Outline each Babesia divergens-infected red blood cell.
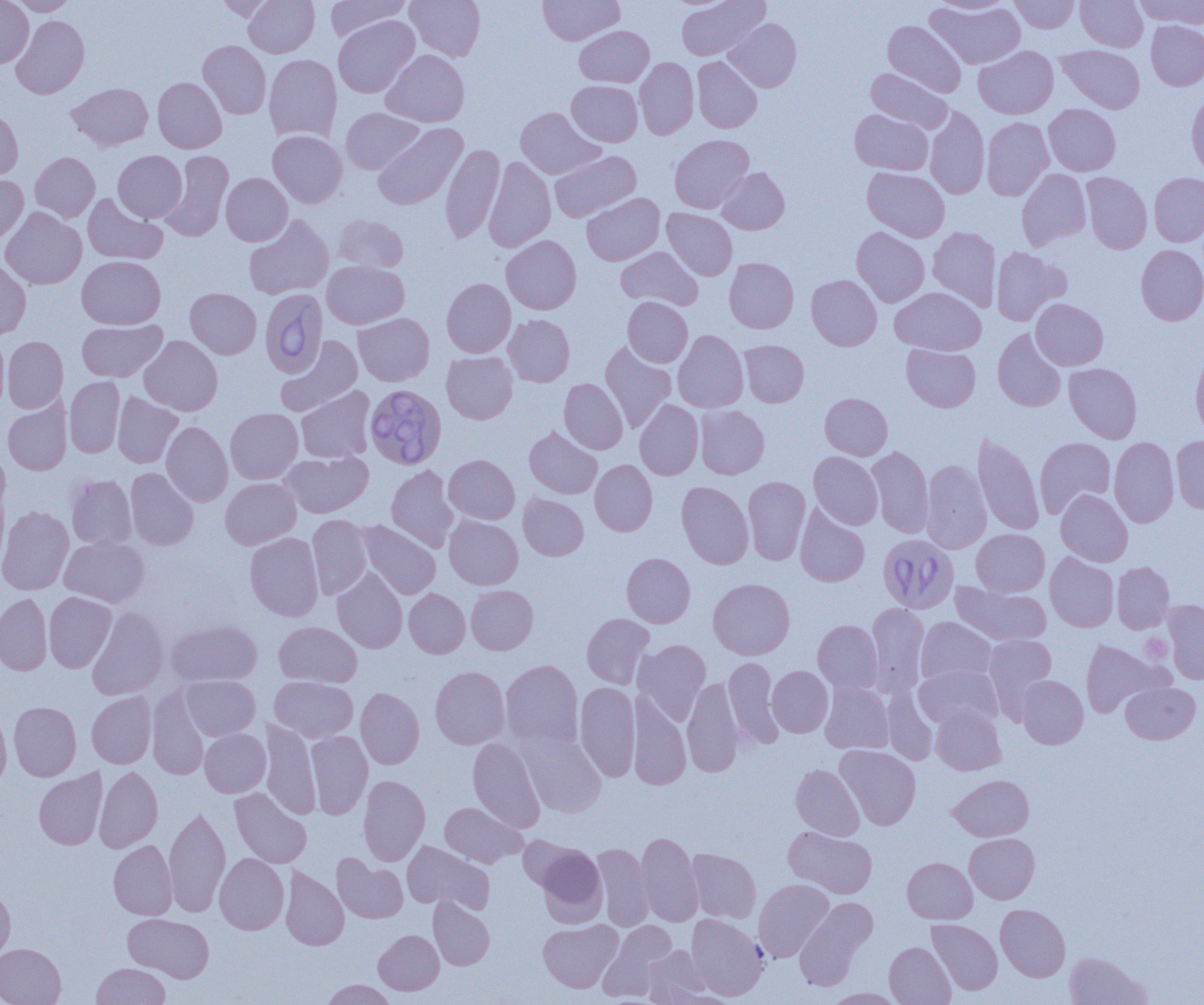
Approximate bounding boxes as (x1,y1)-(x2,y2) corner pairs in pixels.
Babesia divergens-infected red blood cells: (260,288)-(327,378), (365,384)-(446,469), (881,533)-(956,616).

slide-level diagnosis = Babesia divergens
modality = light microscopy
preparation = thin blood film
uninfected red blood cell locations = approximate bounding boxes as (x1,y1)-(x2,y2) corner pairs in pixels: (0,0)-(34,68), (9,0)-(77,15), (214,0)-(279,21), (243,0)-(319,57), (326,0)-(411,41), (405,0)-(485,61), (538,0)-(624,45), (676,0)-(769,60), (933,0)-(1014,14), (1009,0)-(1079,33), (1076,0)-(1148,52), (1134,0)-(1204,29), (925,1)-(1025,69), (11,15)-(90,99), (333,15)-(419,98), (724,18)-(801,92), (883,20)-(966,97), (1146,21)-(1204,90), (574,25)-(654,87), (198,40)-(271,119), (973,45)-(1058,118), (1057,45)-(1145,113), (381,50)-(469,127), (264,54)-(342,143), (692,56)-(762,133), (635,57)-(699,139), (866,69)-(952,133), (153,77)-(226,153), (567,80)-(642,146), (67,82)-(153,151), (1186,93)-(1204,180), (1044,104)-(1121,175), (925,106)-(989,199), (341,107)-(423,174), (515,107)-(604,179), (0,109)-(23,180), (849,109)-(933,175), (982,117)-(1054,200), (372,123)-(467,210), (268,130)-(347,208), (669,135)-(754,213), (441,143)-(505,244), (113,150)-(187,222), (160,150)-(233,242), (550,150)-(641,222), (30,152)-(100,222), (484,156)-(555,253), (717,167)-(789,234), (862,167)-(950,242), (1016,169)-(1091,250), (221,172)-(292,246), (1081,172)-(1152,254), (1149,172)-(1204,246), (0,175)-(28,244), (582,192)-(664,265), (82,193)-(167,265), (0,207)-(87,289), (662,208)-(737,280), (243,214)-(334,300), (334,215)-(409,272), (928,226)-(1001,311), (852,227)-(929,307), (501,235)-(581,315), (1136,244)-(1204,325), (616,246)-(703,310), (991,247)-(1070,325), (77,256)-(166,329), (0,257)-(31,340), (724,257)-(798,333), (322,260)-(409,329), (806,275)-(881,350), (441,278)-(516,357), (890,287)-(986,355), (185,288)-(261,359), (623,296)-(693,367), (1031,299)-(1108,370), (354,313)-(434,386), (504,314)-(574,386), (76,319)-(167,382), (992,329)-(1066,412), (673,330)-(748,413), (0,335)-(10,413), (139,335)-(223,415), (2,336)-(68,413), (275,336)-(362,417), (739,340)-(809,407), (599,341)-(676,432), (902,343)-(980,412), (1191,349)-(1204,438), (441,351)-(517,423), (1064,363)-(1142,443), (64,376)-(125,458), (559,378)-(628,454), (296,386)-(376,463), (113,391)-(183,468), (820,393)-(892,459), (2,398)-(72,475), (635,399)-(703,480), (695,405)-(769,478), (225,408)-(303,484), (161,421)-(233,507), (524,426)-(602,499), (973,433)-(1044,535), (1171,436)-(1204,513), (1035,437)-(1116,518), (1109,437)-(1179,528), (867,446)-(934,538), (281,450)-(373,518), (809,451)-(883,529), (444,454)-(520,524), (921,458)-(991,553), (590,460)-(657,536), (386,465)-(458,552), (125,467)-(199,550), (66,474)-(137,549), (743,476)-(810,564), (220,477)-(301,549), (676,481)-(753,569), (1055,489)-(1132,566), (518,493)-(588,560), (795,504)-(870,587), (0,506)-(74,595), (307,514)-(372,599), (444,515)-(523,590), (357,521)-(440,599), (972,529)-(1049,596), (245,533)-(324,621), (59,535)-(149,607), (622,552)-(695,627), (1045,552)-(1119,632), (1112,561)-(1174,633), (332,569)-(407,653), (708,578)-(795,659), (952,582)-(1052,646), (466,584)-(538,654), (404,588)-(470,658), (44,592)-(116,672), (0,593)-(52,675), (1162,600)-(1204,683), (866,603)-(929,696), (87,606)-(169,700), (581,613)-(654,689), (916,617)-(997,686), (167,619)-(262,687), (813,619)-(882,694), (274,621)-(362,687), (983,633)-(1056,716), (1081,638)-(1166,717), (633,639)-(711,724), (723,657)-(784,748), (500,659)-(584,750), (915,664)-(1002,730), (430,666)-(510,749), (767,666)-(833,737), (180,675)-(260,740), (1017,675)-(1088,748), (270,676)-(358,742), (682,677)-(744,777), (574,681)-(640,781), (820,681)-(894,754), (1121,681)-(1200,743), (147,687)-(211,780), (356,688)-(424,769), (881,689)-(937,765), (87,692)-(156,768), (628,692)-(691,789), (9,701)-(81,781), (931,705)-(1005,775), (0,709)-(12,791), (259,720)-(321,819), (200,728)-(270,797), (519,730)-(606,818), (306,731)-(372,819), (468,737)-(545,833), (835,745)-(921,829), (791,764)-(864,840), (94,766)-(163,852), (34,768)-(107,850), (359,775)-(430,866), (948,775)-(1034,841), (229,787)-(311,868), (440,802)-(527,867), (164,806)-(231,916), (783,826)-(877,898), (636,832)-(703,926), (964,833)-(1039,903), (518,835)-(582,892), (109,840)-(177,920), (403,841)-(494,914), (535,843)-(606,923), (592,843)-(654,931), (686,848)-(761,923), (215,853)-(289,934), (332,854)-(408,923), (902,857)-(977,923), (280,867)-(349,950), (753,879)-(834,962), (0,884)-(15,964), (428,897)-(494,969), (794,897)-(877,989), (995,904)-(1070,981), (686,913)-(768,1000), (123,914)-(214,982), (538,919)-(622,992), (927,919)-(1002,995), (598,920)-(677,1000), (374,930)-(444,995), (884,942)-(955,1005), (0,943)-(66,1005), (643,946)-(712,1005), (1065,951)-(1152,1005), (92,963)-(170,1005), (322,979)-(395,1005), (824,988)-(904,1004), (664,991)-(742,1005)
magnification = 1000x
image size = 1204×1005 pixels
field of view = one of a larger specimen
platelet locations = approximate bounding boxes as (x1,y1)-(x2,y2) corner pairs in pixels: (1139,633)-(1173,662)